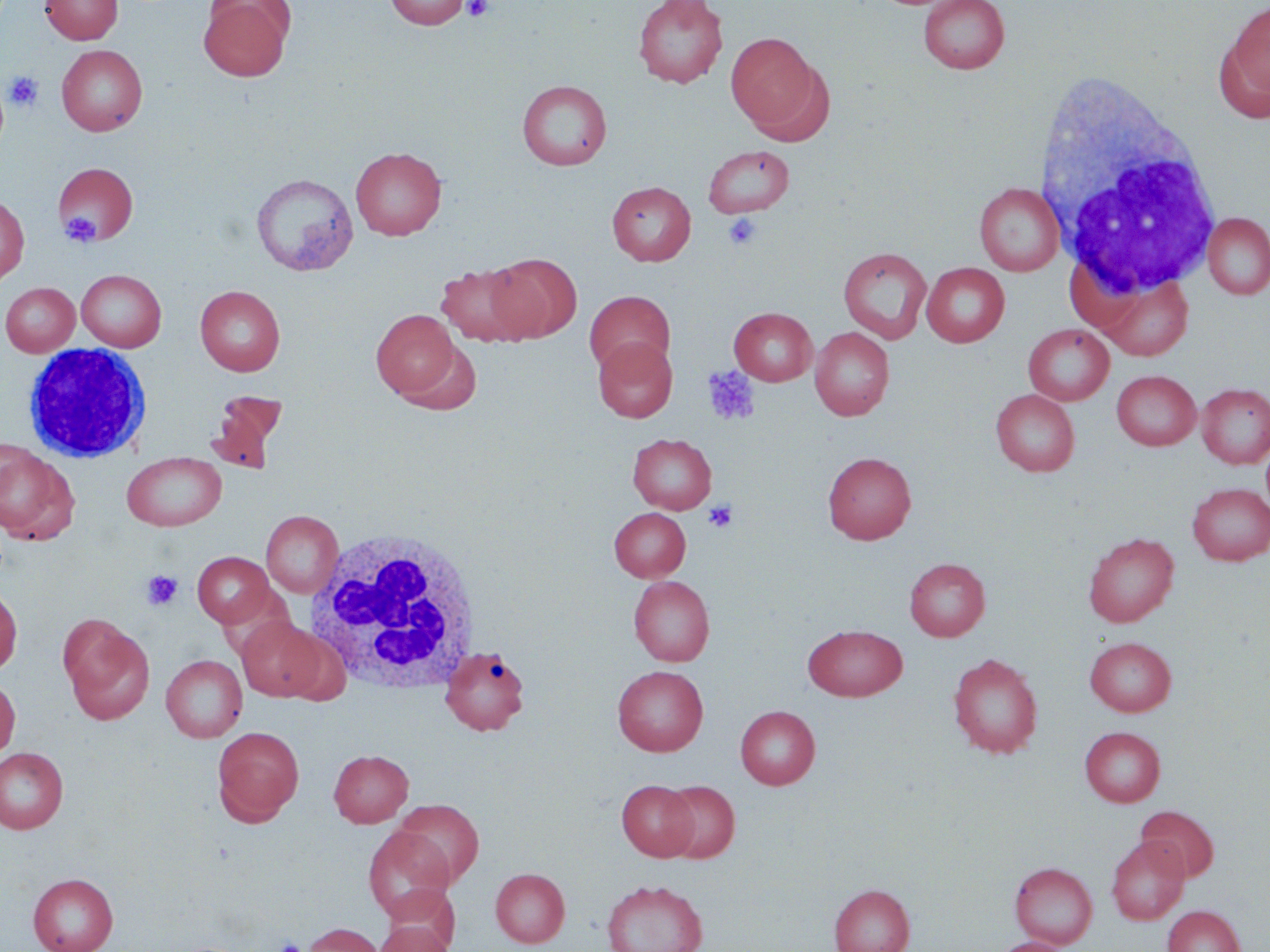
slide-level diagnosis = negative for blood parasites
preparation = thin blood smear
field of view = single
white blood cell locations = approximate bounding boxes as [x1, y1, x2, y2] in pixels: [1040, 84, 1224, 301], [22, 343, 152, 463], [305, 528, 481, 693]
platelet locations = approximate bounding boxes as [x1, y1, x2, y2] in pixels: [462, 0, 494, 21], [4, 71, 43, 112], [60, 211, 101, 246], [723, 213, 763, 250], [702, 365, 761, 427], [703, 499, 738, 533], [142, 570, 182, 610], [275, 938, 303, 952]
stain = May-Grünwald-Giemsa
modality = light microscopy
magnification = 1000x
image size = 1270×952 pixels
uninfected red blood cell locations = approximate bounding boxes as [x1, y1, x2, y2] in pixels: [40, 0, 123, 44], [199, 0, 293, 81], [385, 0, 470, 30], [632, 0, 728, 88], [918, 0, 1009, 74], [1223, 1, 1270, 113], [726, 32, 818, 129], [57, 45, 147, 136], [748, 63, 836, 147], [517, 79, 611, 169], [703, 145, 794, 217], [350, 146, 446, 240], [53, 162, 137, 246], [251, 173, 358, 276], [607, 181, 696, 265], [974, 183, 1064, 276], [0, 193, 29, 285], [1202, 213, 1270, 300], [838, 247, 932, 343], [485, 253, 581, 342], [435, 261, 535, 347], [921, 262, 1010, 347], [76, 269, 167, 351], [1096, 274, 1194, 360], [1, 282, 80, 356], [195, 285, 284, 376], [584, 290, 674, 377], [729, 307, 817, 385], [371, 310, 460, 399], [1023, 324, 1114, 405], [810, 327, 894, 420], [593, 337, 677, 422], [395, 340, 482, 416], [1111, 370, 1201, 450], [1196, 383, 1270, 468], [991, 389, 1079, 476], [210, 391, 286, 471], [628, 433, 716, 514], [0, 443, 79, 545], [122, 452, 226, 531], [823, 452, 917, 544], [1187, 483, 1270, 565], [609, 508, 690, 581], [261, 510, 343, 597], [1083, 532, 1178, 627], [193, 552, 273, 627], [904, 557, 990, 641], [629, 576, 715, 666], [0, 584, 22, 675], [59, 614, 155, 725], [236, 617, 327, 701], [803, 625, 907, 701], [1085, 636, 1176, 716], [440, 646, 530, 735], [948, 653, 1044, 758], [160, 655, 247, 742], [613, 665, 708, 756], [0, 677, 19, 760], [736, 705, 820, 789], [212, 726, 304, 825], [1080, 726, 1165, 807], [0, 747, 68, 834], [329, 749, 413, 827], [617, 779, 699, 860], [659, 780, 740, 862], [393, 799, 484, 887], [1136, 805, 1219, 881], [363, 827, 454, 920], [1107, 836, 1189, 925], [1010, 862, 1097, 948], [490, 867, 570, 947], [28, 873, 118, 952], [601, 879, 708, 952], [829, 884, 915, 952], [379, 886, 460, 950], [1162, 905, 1245, 952], [373, 920, 455, 952], [301, 922, 385, 952], [993, 937, 1072, 952]